Name the parasite shown.
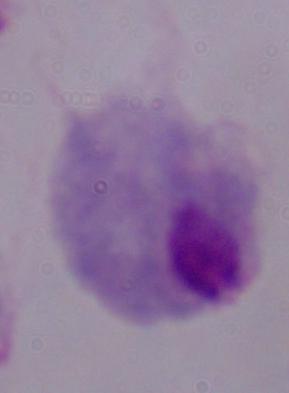

A trichomonad.

modality = photomicrograph
magnification = 1000x